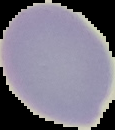
From a thin blood smear. The area outside the segmented cell region is set to black. Image is 115×130 pixels. Result: no Plasmodium parasites detected.